Name the blood parasite species.
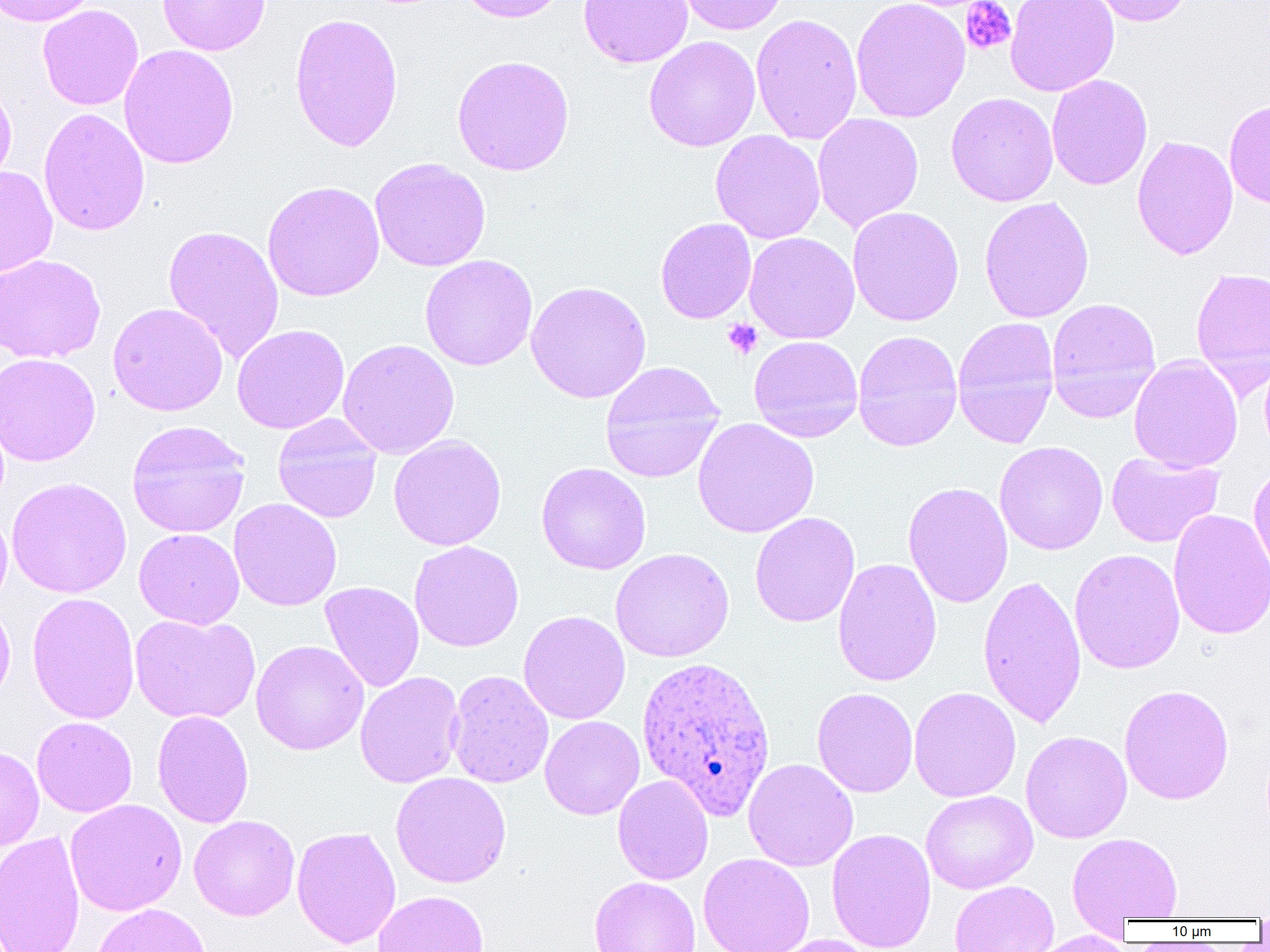
Plasmodium ovale.

Summary:
  - Coordinate format: approximate bounding boxes as (x1,y1)-(x2,y2) corner pairs in pixels
  - Uninfected red blood cell locations: (0,0)-(100,27), (158,0)-(271,56), (458,0)-(569,23), (578,0)-(693,68), (676,0)-(788,35), (850,0)-(971,123), (1005,0)-(1119,97), (1086,0)-(1193,26), (37,5)-(143,110), (289,12)-(404,152), (750,13)-(863,145), (643,36)-(761,152), (118,44)-(239,169), (451,54)-(574,176), (1046,74)-(1152,190), (0,81)-(17,192), (946,92)-(1059,207), (1225,99)-(1270,208), (38,107)-(150,236), (812,112)-(924,233), (710,130)-(826,244), (1132,135)-(1238,260), (370,157)-(491,272), (0,165)-(57,278), (262,180)-(384,302), (978,196)-(1095,324), (847,206)-(964,327), (655,217)-(756,324), (162,224)-(285,364), (744,232)-(860,344), (0,254)-(106,363), (419,255)-(538,371), (1190,267)-(1270,391), (526,281)-(651,403), (1046,297)-(1161,421), (107,302)-(228,416), (952,316)-(1060,449), (232,324)-(350,434), (852,329)-(963,452), (748,336)-(864,443), (337,338)-(459,460), (0,352)-(100,466), (1259,353)-(1270,461), (1129,354)-(1243,473), (600,361)-(725,483), (272,414)-(383,523), (692,417)-(819,538), (127,420)-(250,538), (388,434)-(507,551), (994,441)-(1108,555), (1106,452)-(1224,548), (1248,461)-(1270,581), (536,462)-(651,575), (6,477)-(132,597), (902,481)-(1013,608), (228,498)-(342,611), (0,507)-(12,611), (1167,508)-(1270,641), (749,512)-(860,628), (133,527)-(245,629), (409,540)-(524,652), (610,548)-(734,662), (1069,548)-(1185,675), (832,558)-(942,687), (977,573)-(1087,729), (320,581)-(424,693), (26,592)-(140,725), (0,596)-(16,709), (518,610)-(630,724), (129,614)-(260,724), (251,640)-(369,755), (446,669)-(553,789), (355,671)-(465,788), (1119,684)-(1235,805), (812,687)-(918,798), (908,687)-(1021,802), (152,709)-(254,828), (32,716)-(137,817), (540,716)-(644,820), (1020,731)-(1132,843), (0,745)-(44,851), (743,758)-(859,871), (390,772)-(511,888), (612,774)-(713,885), (920,790)-(1038,894), (65,798)-(187,916), (188,815)-(300,921), (291,826)-(401,949), (826,828)-(936,952), (0,831)-(86,952), (1068,832)-(1183,923), (699,853)-(814,952), (589,876)-(701,952), (949,880)-(1059,952), (372,890)-(489,952), (91,903)-(211,952), (1026,930)-(1135,952), (767,934)-(878,952)
  - Plasmodium ovale-infected red blood cell locations: (636,655)-(777,820)
  - Platelet locations: (961,0)-(1016,55), (722,318)-(763,360)
  - Image size: 1270×952 pixels
  - Preparation: thin blood smear
  - Magnification: 1000x
  - Field of view: one of a larger specimen
  - Modality: light microscopy